Give the extent of all Plasmodium ovale-infected red blood cells.
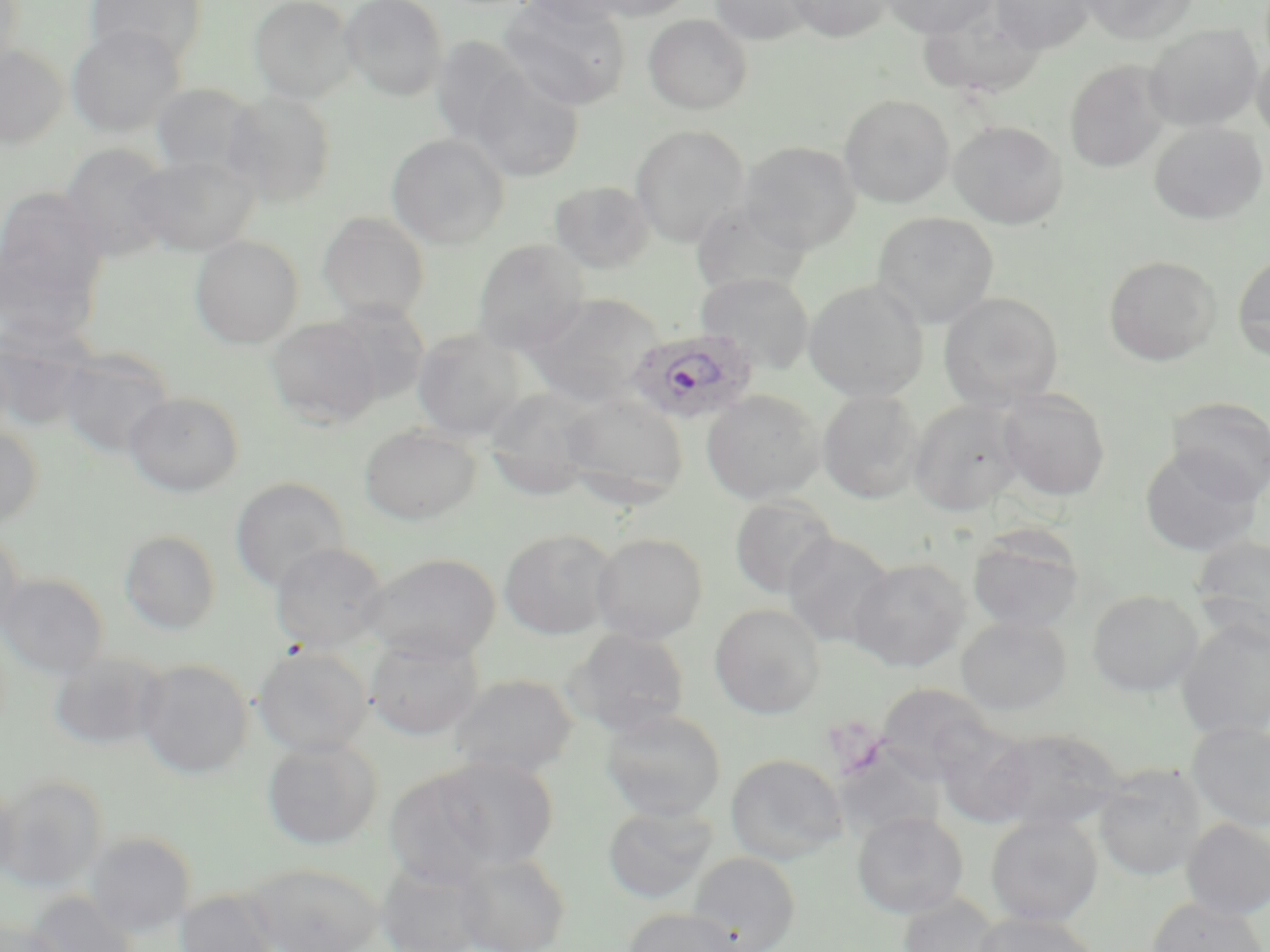
Approximate bounding boxes as (x1, y1, x2, y2) in pixels.
Plasmodium ovale-infected red blood cells: (626, 327, 760, 426).

Summary:
  - Uninfected red blood cell locations: (0, 0, 25, 72), (85, 0, 209, 67), (248, 0, 356, 103), (339, 0, 448, 101), (499, 0, 631, 110), (519, 0, 633, 27), (584, 0, 697, 21), (710, 0, 814, 45), (786, 0, 892, 42), (881, 0, 996, 38), (990, 0, 1095, 53), (1079, 0, 1198, 44), (919, 6, 1045, 98), (644, 14, 752, 114), (1145, 24, 1262, 131), (66, 25, 184, 137), (431, 37, 533, 146), (0, 44, 68, 149), (1252, 45, 1270, 144), (1065, 59, 1171, 172), (467, 65, 586, 182), (150, 83, 261, 179), (224, 91, 338, 206), (839, 94, 955, 208), (949, 120, 1068, 228), (1149, 121, 1268, 225), (630, 125, 749, 247), (386, 134, 509, 250), (739, 140, 861, 253), (58, 143, 176, 261), (129, 154, 259, 256), (550, 180, 655, 273), (0, 187, 108, 303), (690, 200, 811, 297), (318, 212, 430, 322), (872, 212, 998, 328), (190, 235, 304, 349), (472, 240, 590, 355), (0, 241, 102, 354), (1233, 249, 1270, 362), (1104, 255, 1221, 365), (695, 273, 815, 373), (804, 280, 928, 402), (526, 292, 664, 406), (939, 292, 1065, 411), (325, 301, 430, 404), (267, 317, 384, 428), (1, 319, 99, 430), (412, 329, 526, 441), (56, 347, 177, 460), (484, 387, 600, 499), (701, 389, 825, 504), (817, 389, 924, 503), (997, 389, 1111, 501), (124, 391, 244, 497), (558, 392, 689, 508), (1166, 396, 1270, 501), (908, 400, 1026, 515), (0, 423, 43, 529), (360, 424, 481, 524), (1141, 447, 1262, 556), (230, 477, 349, 593), (729, 495, 839, 600), (966, 527, 1086, 633), (0, 528, 25, 638), (499, 529, 617, 639), (120, 530, 221, 635), (591, 532, 708, 643), (782, 532, 896, 648), (1190, 535, 1270, 649), (270, 542, 390, 653), (361, 552, 502, 662), (848, 557, 972, 672), (1, 573, 109, 678), (1087, 589, 1204, 696), (710, 603, 825, 719), (956, 614, 1072, 715), (1176, 618, 1270, 740), (567, 628, 691, 735), (365, 636, 484, 740), (253, 646, 373, 757), (47, 652, 167, 752), (135, 659, 254, 779), (448, 674, 579, 778), (875, 683, 997, 782), (600, 707, 726, 822), (1186, 720, 1270, 832), (933, 721, 1037, 828), (986, 726, 1127, 832), (262, 738, 383, 850), (831, 746, 948, 843), (726, 753, 849, 864), (432, 756, 559, 871), (1093, 765, 1207, 881), (383, 767, 507, 887), (0, 775, 108, 891), (0, 779, 21, 881), (603, 803, 716, 903), (852, 811, 969, 918), (985, 814, 1103, 926), (1181, 819, 1270, 919), (84, 831, 196, 937), (688, 851, 801, 952), (454, 852, 571, 952), (245, 862, 382, 952), (375, 862, 490, 952), (175, 888, 280, 952), (25, 890, 140, 951), (896, 892, 1005, 952), (1147, 896, 1268, 952), (622, 907, 744, 952), (971, 912, 1100, 952), (0, 920, 68, 952)
  - Slide-level diagnosis: Plasmodium ovale
  - Image size: 1270×952 pixels
  - Stain: May-Grünwald-Giemsa
  - Magnification: 1000x
  - Preparation: thin blood smear
  - Modality: light microscopy
  - Field of view: single